Name the parasite shown.
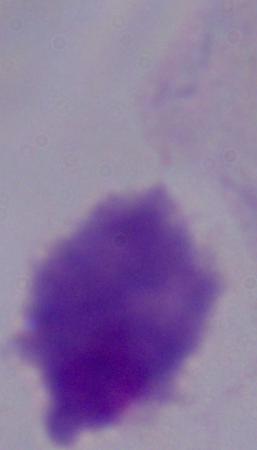
A trichomonad.

Micrograph. 1000x magnification.